Classify this cell by malaria status.
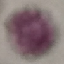

It is uninfected.

preparation = thin blood smear
capture = smartphone camera at the microscope eyepiece
stain = Giemsa
image type = automatically extracted cell patch, resized to 64 × 64 pixels